State which cell type is depicted.
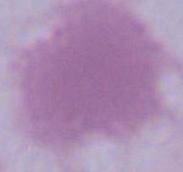

This is an erythrocyte.

1000x magnification. Micrograph.